Identify the cell.
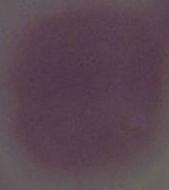

An erythrocyte.

Captured at 1000x magnification. Micrograph.